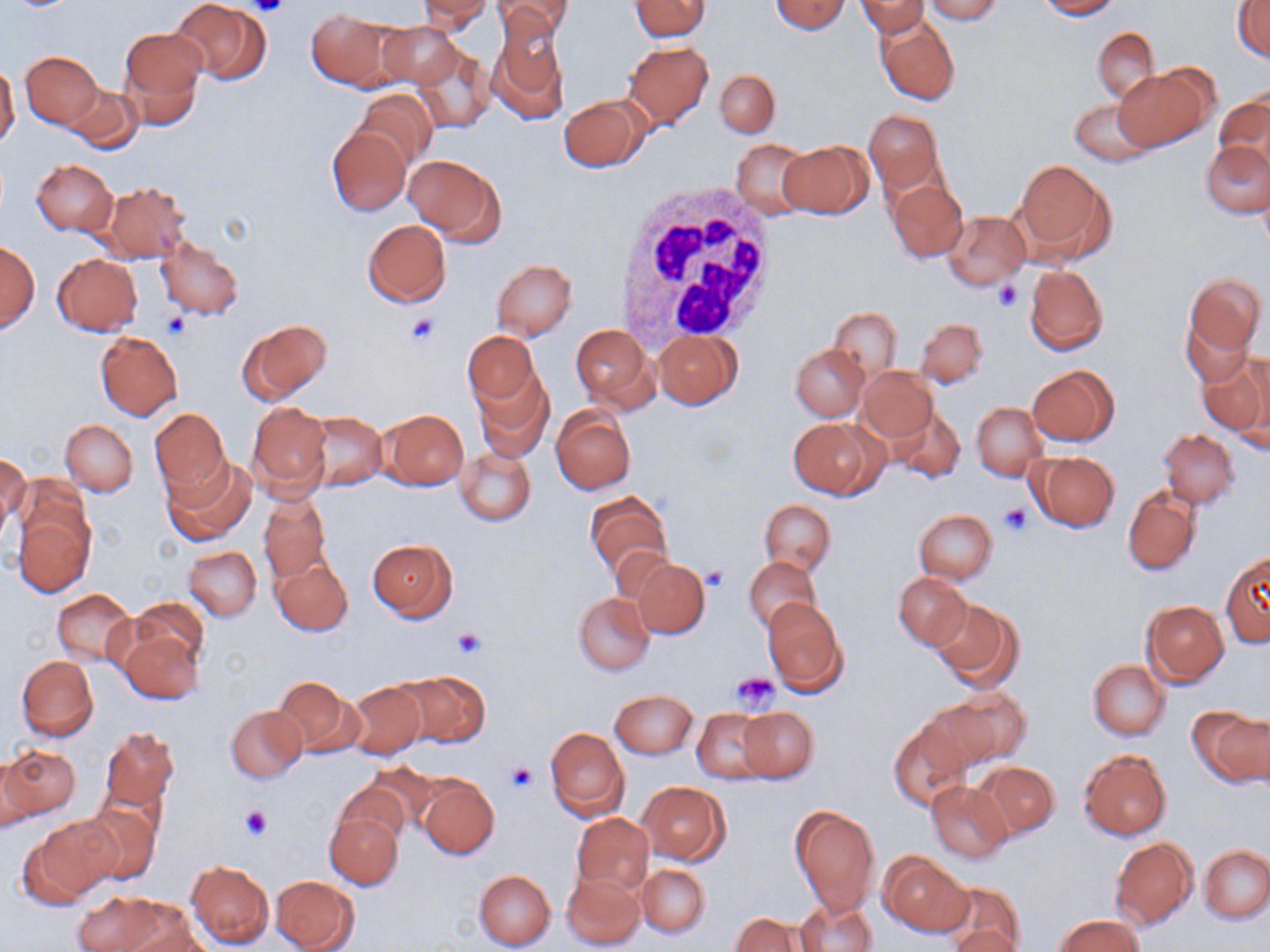

Approximate bounding boxes as (x1, y1, x2, y2) in pixels. White blood cell locations: (617, 183, 784, 347). Uninfected red blood cell locations: (169, 0, 270, 84), (493, 0, 573, 44), (629, 0, 710, 40), (771, 0, 849, 35), (858, 0, 927, 39), (921, 0, 1003, 23), (1034, 0, 1122, 19), (416, 1, 492, 33), (1233, 3, 1270, 63), (305, 7, 396, 90), (875, 16, 960, 107), (488, 19, 569, 122), (374, 22, 461, 92), (119, 26, 207, 127), (1091, 26, 1160, 103), (624, 41, 713, 127), (408, 43, 495, 134), (20, 51, 102, 129), (0, 64, 20, 149), (1114, 67, 1211, 151), (715, 69, 779, 137), (63, 85, 142, 154), (353, 89, 435, 168), (1215, 91, 1270, 173), (559, 95, 649, 171), (1069, 98, 1155, 165), (863, 109, 943, 193), (326, 127, 410, 215), (733, 138, 812, 220), (779, 141, 873, 219), (1202, 142, 1269, 217), (404, 154, 505, 240), (1012, 158, 1115, 265), (32, 159, 117, 236), (886, 177, 967, 264), (99, 181, 191, 261), (941, 211, 1029, 290), (363, 220, 451, 307), (155, 238, 244, 319), (1, 242, 40, 333), (52, 253, 143, 336), (492, 259, 576, 339), (1025, 265, 1108, 357), (1185, 274, 1264, 358), (827, 307, 901, 380), (1180, 311, 1256, 390), (915, 317, 988, 388), (238, 319, 332, 404), (570, 324, 655, 408), (95, 331, 182, 421), (463, 331, 540, 407), (654, 331, 743, 409), (791, 344, 867, 420), (1198, 351, 1269, 440), (1238, 353, 1270, 451), (1026, 365, 1119, 445), (857, 367, 937, 444), (474, 370, 553, 459), (247, 401, 331, 499), (972, 402, 1046, 481), (149, 407, 231, 496), (885, 407, 966, 483), (378, 408, 469, 489), (551, 408, 635, 494), (305, 411, 386, 490), (790, 417, 885, 499), (61, 419, 137, 496), (1158, 429, 1240, 507), (455, 447, 536, 525), (1028, 451, 1119, 531), (1, 453, 28, 537), (162, 458, 256, 548), (1123, 487, 1201, 576), (584, 491, 673, 583), (259, 492, 331, 583), (760, 500, 835, 576), (11, 502, 95, 598), (915, 509, 998, 584), (368, 538, 458, 619), (184, 545, 261, 621), (1221, 552, 1270, 647), (744, 555, 821, 634), (270, 556, 353, 636), (627, 558, 710, 639), (894, 572, 970, 649), (52, 589, 135, 664), (574, 592, 654, 674), (762, 597, 848, 696), (929, 597, 1022, 689), (130, 598, 209, 671), (1141, 600, 1229, 687), (117, 626, 204, 706), (17, 655, 99, 740), (1088, 659, 1170, 739), (395, 670, 490, 747), (272, 677, 364, 757), (344, 683, 425, 758), (936, 686, 1031, 764), (611, 690, 698, 758), (226, 704, 307, 783), (1191, 704, 1270, 788), (738, 706, 818, 782), (692, 708, 771, 784), (889, 718, 972, 810), (99, 725, 180, 814), (545, 727, 630, 820), (0, 745, 80, 824), (1079, 750, 1172, 839), (975, 760, 1060, 837), (416, 775, 498, 859), (925, 780, 1014, 863), (333, 781, 411, 848), (638, 782, 729, 864), (75, 800, 160, 886), (790, 805, 880, 913), (325, 812, 403, 890), (572, 813, 653, 894), (19, 816, 116, 907), (1109, 837, 1198, 930), (1199, 845, 1269, 923), (881, 853, 972, 934), (185, 860, 273, 949), (636, 864, 710, 938), (473, 869, 556, 950), (562, 872, 645, 949), (270, 874, 361, 952), (938, 882, 1026, 952), (74, 892, 165, 951), (795, 899, 876, 952), (113, 900, 208, 951), (731, 913, 804, 952), (1055, 915, 1143, 952), (949, 926, 1026, 952). Platelet locations: (249, 0, 289, 18), (991, 280, 1022, 312), (162, 312, 192, 340), (406, 313, 440, 346), (998, 503, 1032, 537), (702, 565, 729, 590), (453, 627, 488, 659), (732, 671, 780, 712), (506, 760, 537, 793), (240, 804, 271, 840). Slide-level diagnosis: negative for blood parasites. Light microscopy. Thin blood film. May-Grünwald-Giemsa stain. Image is 1270×952 pixels. Captured at 1000x magnification. Single field of view.